Assess this cell for malaria.
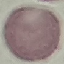

Uninfected.

Acquired by smartphone through the microscope eyepiece. Cell patch, automatically extracted from a larger field of view and resized to 64 × 64 pixels. Giemsa stain. Thin blood film.